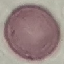 Malaria status: uninfected. Thin blood smear. Cell patch, automatically extracted from a larger field of view and resized to 64 × 64 pixels. Photographed with a smartphone camera at the microscope eyepiece. Giemsa stain.